State which cell type is depicted.
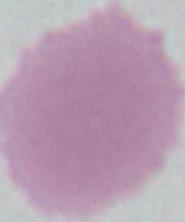

This is an erythrocyte.

Summary:
  - Modality: micrograph
  - Magnification: 1000x